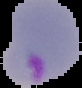
Malaria status: parasitized. Image is 82×88 pixels. The area outside the segmented cell region is set to black. From a thin blood film.